State which parasite is depicted.
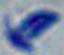

Toxoplasma gondii.

magnification = 1000x
modality = photomicrograph